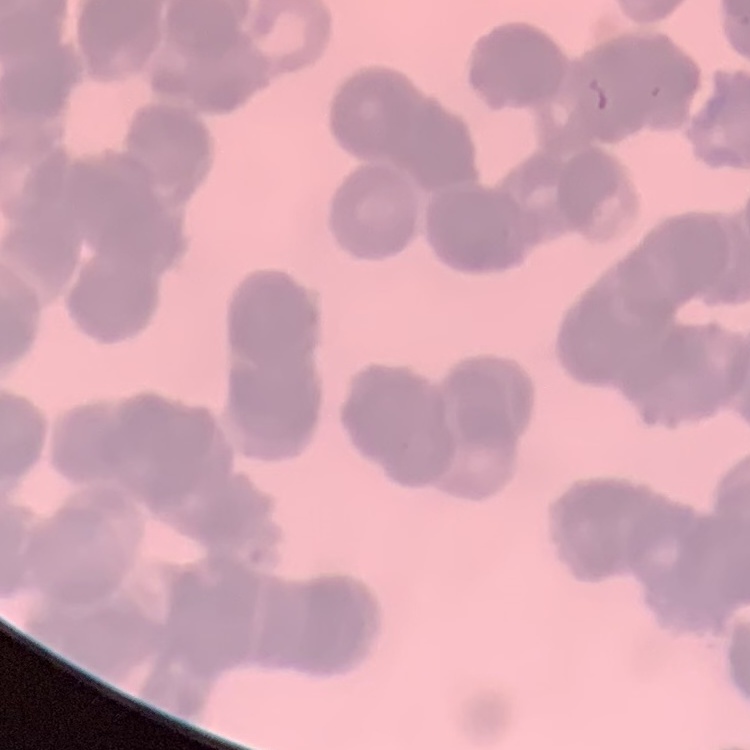
red blood cell morphology = rouleaux formation
preparation = thin blood film
stain = Field's or Giemsa
image type = square crop of a larger photomicrograph